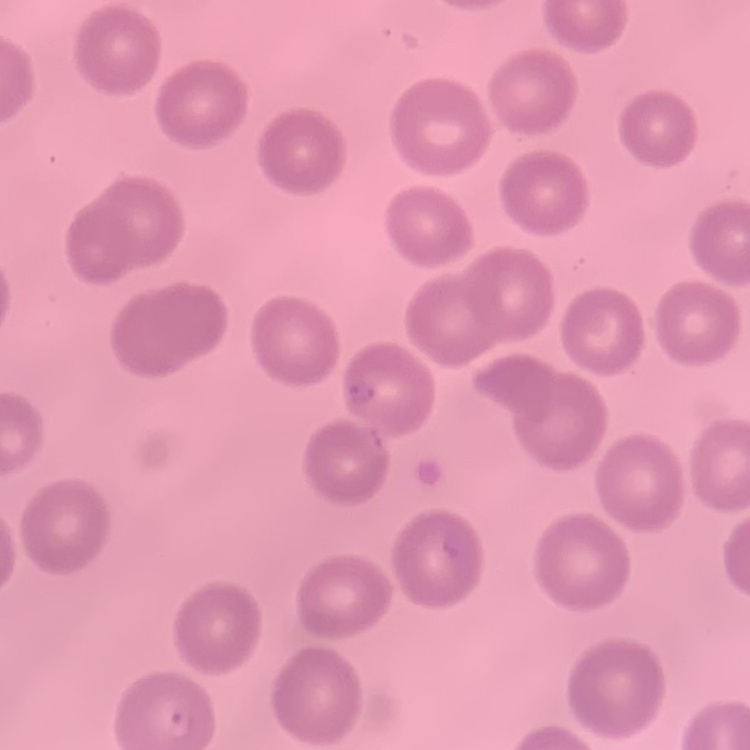
The erythrocytes show no rouleaux formation. Thin peripheral smear. One tile cut from a larger photomicrograph. Stained with either Field's or Giemsa.